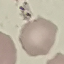
Summary:
  - Malaria status: uninfected
  - Stain: Giemsa
  - Capture: smartphone through the microscope eyepiece
  - Preparation: thin blood film
  - Image type: cell patch, automatically extracted from a larger field of view and resized to 64 × 64 pixels